State the preparation type.
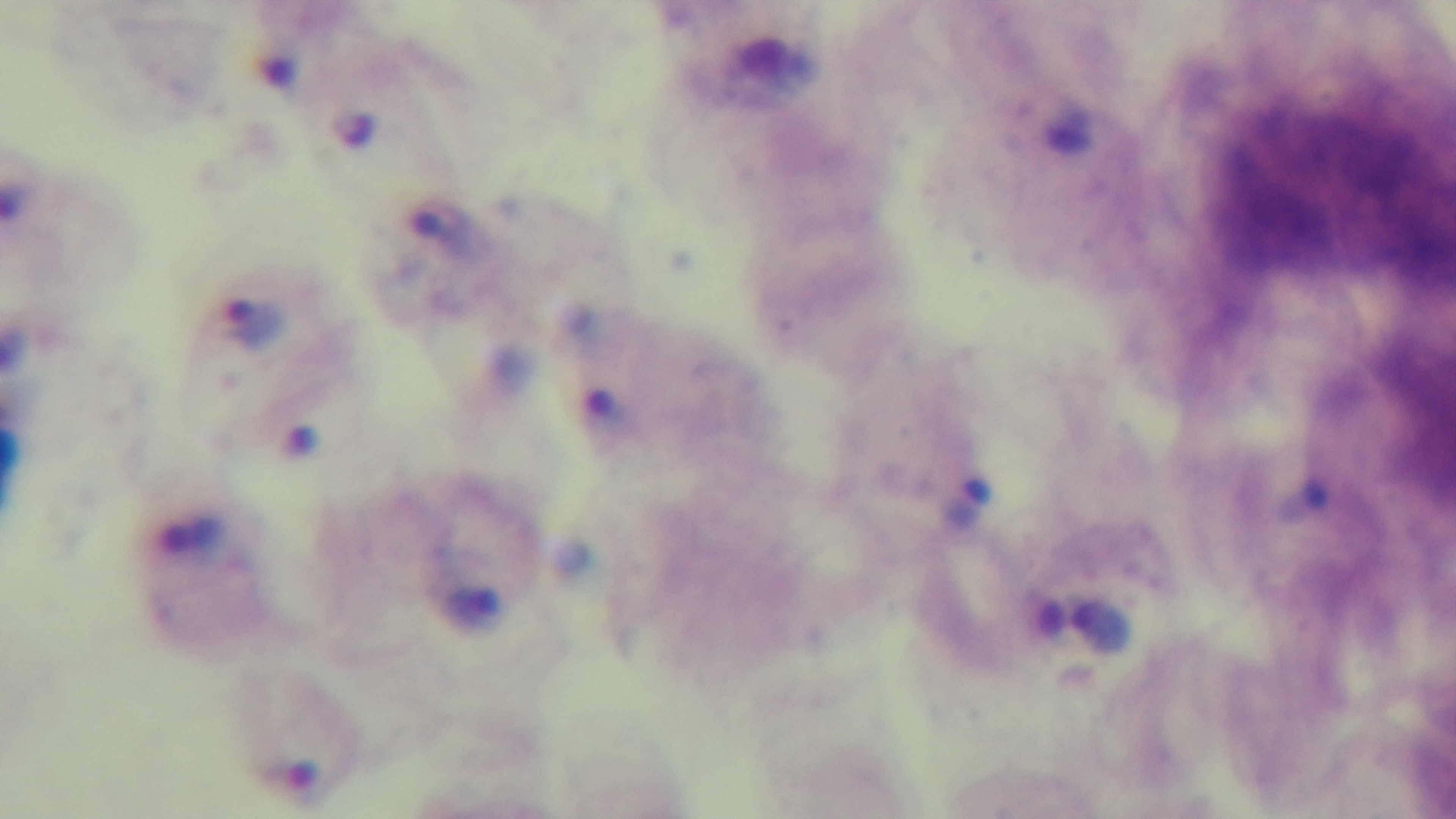

Thick.

One field from the slide. Light microscopy. Malaria status: infected. Oil-immersion objective, 100x. Giemsa stain. Mounted 4K digital camera.